Give the extent of all uninfected red blood cells.
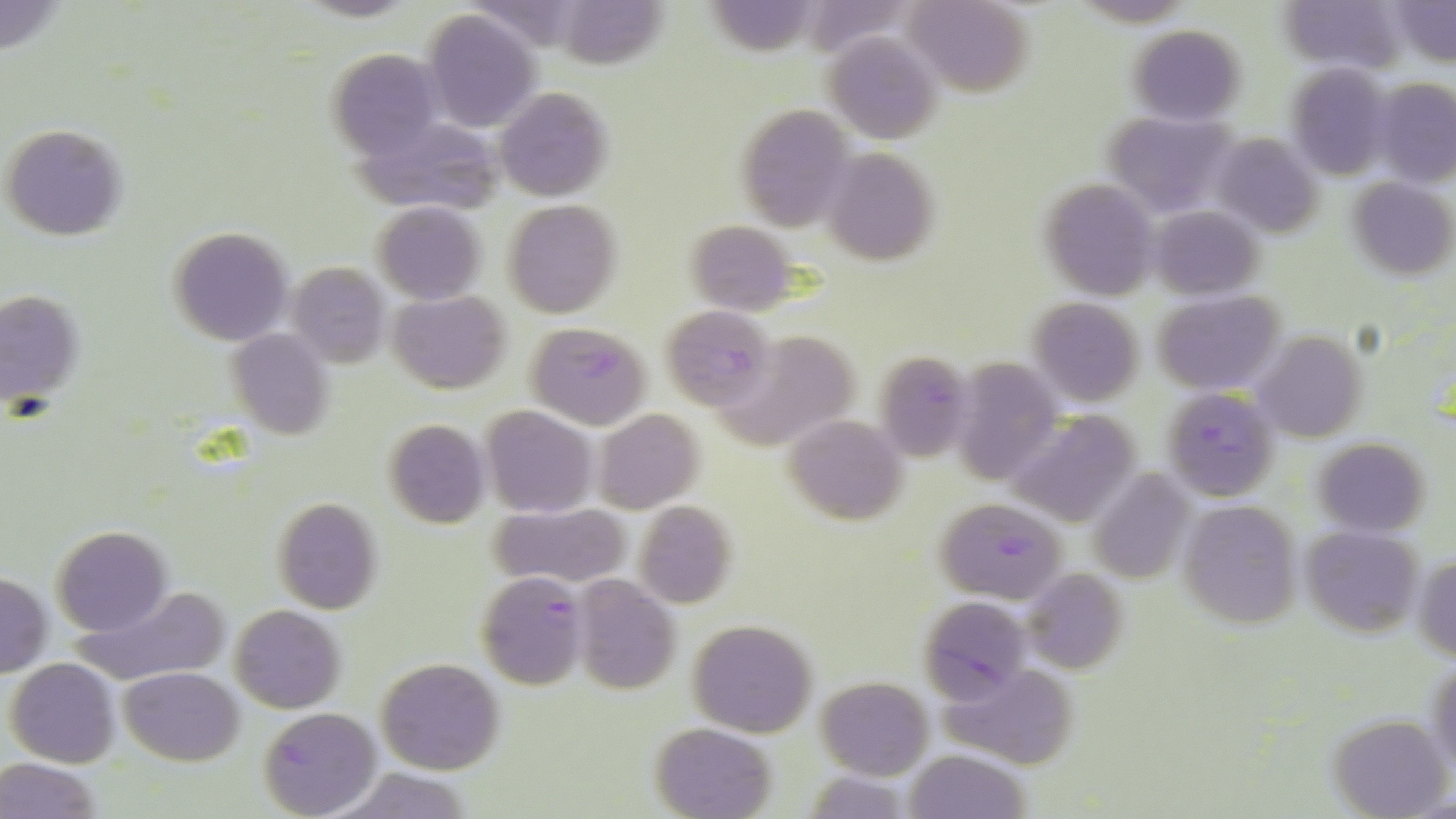
Approximate bounding boxes as [x1, y1, x2, y2] in pixels.
Uninfected red blood cells: [906, 0, 1035, 96], [1280, 0, 1403, 72], [1388, 0, 1456, 66], [422, 9, 541, 132], [1128, 24, 1245, 124], [824, 33, 940, 145], [324, 48, 448, 159], [1287, 65, 1392, 182], [1373, 78, 1456, 186], [495, 87, 613, 200], [732, 104, 852, 230], [1103, 110, 1238, 215], [2, 125, 127, 241], [1211, 134, 1320, 239], [824, 148, 939, 265], [1346, 177, 1455, 279], [1039, 180, 1159, 300], [502, 201, 621, 318], [372, 202, 484, 303], [1150, 204, 1263, 300], [683, 219, 799, 314], [167, 226, 295, 347], [286, 263, 391, 367], [1, 287, 87, 411], [388, 291, 511, 394], [1154, 291, 1284, 396], [1027, 298, 1144, 405], [226, 329, 335, 440], [714, 330, 863, 450], [1252, 330, 1368, 443], [951, 359, 1062, 484], [482, 405, 597, 517], [593, 408, 704, 513], [1005, 410, 1145, 526], [784, 413, 910, 524], [383, 419, 490, 530], [1313, 437, 1431, 536], [1088, 470, 1194, 587], [273, 498, 383, 612], [634, 500, 738, 609], [1177, 500, 1305, 629], [490, 503, 632, 588], [52, 526, 171, 636], [1301, 527, 1422, 639], [1413, 553, 1456, 662], [1022, 568, 1128, 676], [0, 573, 51, 677], [571, 577, 681, 696], [71, 584, 230, 688], [230, 604, 345, 713], [686, 619, 817, 736], [1426, 653, 1456, 777], [375, 657, 504, 775], [6, 658, 121, 768], [936, 659, 1076, 767], [118, 666, 246, 766], [816, 677, 934, 779], [1327, 714, 1451, 818], [650, 721, 776, 819], [905, 749, 1030, 819], [0, 757, 103, 819], [324, 767, 480, 819], [800, 771, 917, 817].

Summary:
  - Plasmodium falciparum-infected red blood cell locations: [659, 306, 773, 410], [525, 321, 651, 429], [874, 351, 973, 456], [1161, 387, 1280, 501], [936, 498, 1064, 601], [474, 572, 587, 691], [918, 597, 1032, 702], [256, 708, 380, 819]
  - Slide-level diagnosis: Plasmodium falciparum
  - Stain: May-Grünwald-Giemsa
  - Modality: optical microscopy
  - Magnification: 1000x
  - Preparation: thin blood film
  - Image size: 1456×819 pixels
  - Field of view: one of a larger specimen